Locate every blood parasite and identify its species.
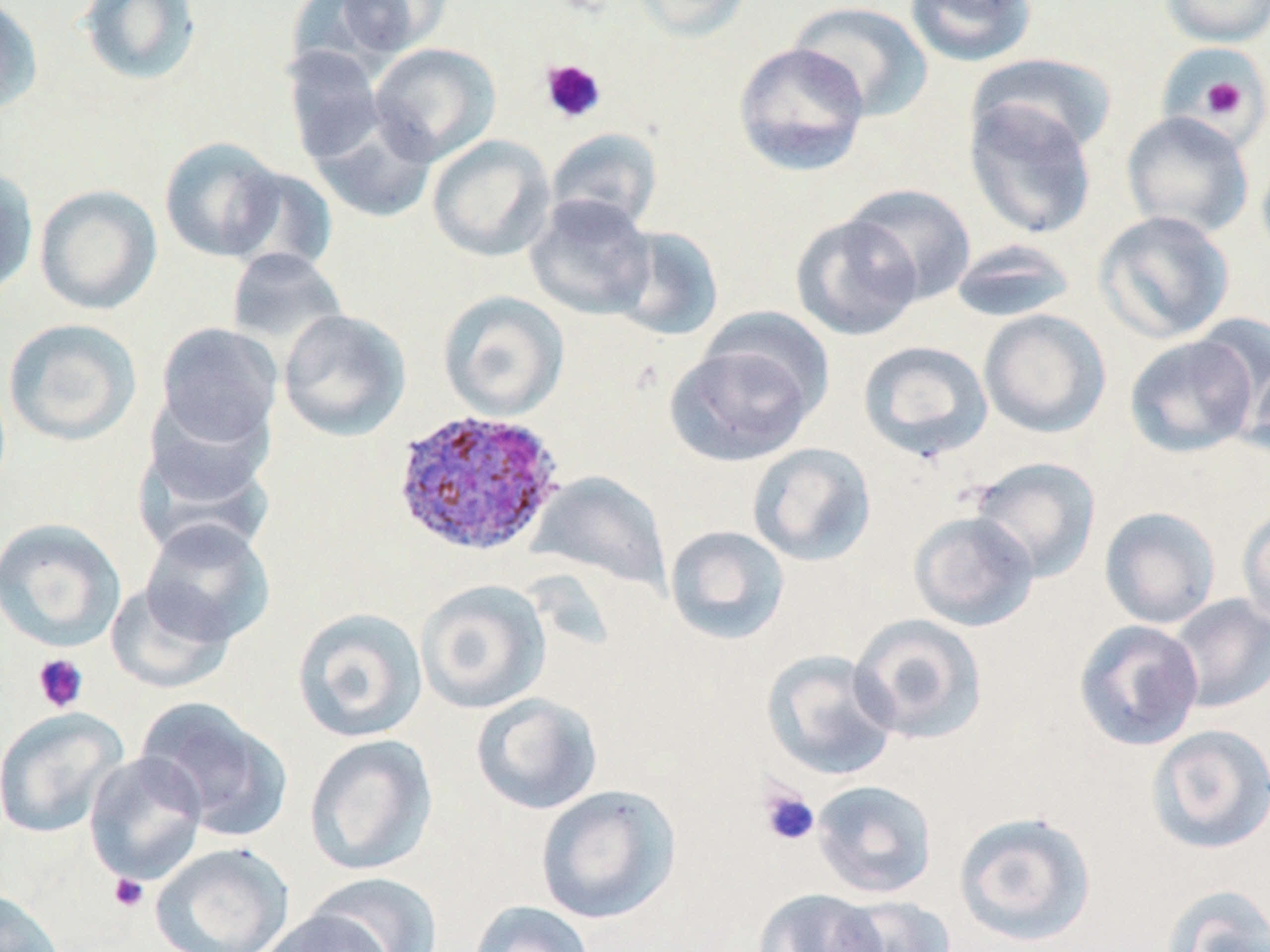

Approximate bounding boxes as (x1, y1, x2, y2) in pixels.
Plasmodium ovale-infected red blood cells: (391, 407, 566, 557).
No Plasmodium falciparum, Plasmodium malariae, Plasmodium vivax, Babesia divergens, or Trypanosoma brucei observed.

slide-level diagnosis = Plasmodium ovale
image size = 1270×952 pixels
magnification = 1000x
platelet locations = approximate bounding boxes as (x1, y1, x2, y2) in pixels: (539, 58, 606, 125), (1197, 75, 1250, 120), (31, 653, 89, 713), (758, 786, 820, 847), (109, 873, 149, 912)
uninfected red blood cell locations = approximate bounding boxes as (x1, y1, x2, y2) in pixels: (76, 0, 202, 87), (333, 0, 450, 58), (630, 0, 754, 42), (904, 0, 1037, 67), (1159, 0, 1270, 47), (0, 1, 43, 117), (787, 1, 933, 122), (369, 42, 501, 165), (733, 42, 870, 177), (282, 46, 387, 164), (1158, 48, 1270, 139), (969, 52, 1118, 158), (963, 97, 1099, 241), (307, 108, 437, 223), (1121, 111, 1255, 239), (545, 127, 663, 233), (427, 135, 556, 262), (159, 136, 285, 262), (1256, 147, 1270, 264), (226, 166, 339, 276), (0, 167, 38, 299), (34, 184, 162, 315), (843, 184, 976, 305), (524, 194, 657, 320), (1094, 210, 1236, 344), (790, 214, 924, 341), (607, 225, 725, 342), (949, 239, 1078, 324), (224, 247, 350, 356), (437, 290, 569, 420), (697, 306, 835, 430), (278, 308, 411, 441), (978, 309, 1111, 438), (1192, 314, 1270, 430), (2, 317, 142, 446), (154, 322, 283, 450), (1124, 332, 1261, 458), (666, 337, 820, 466), (857, 339, 993, 462), (1242, 358, 1270, 459), (136, 401, 278, 534), (747, 442, 876, 567), (967, 456, 1101, 583), (527, 471, 672, 592), (1098, 506, 1222, 629), (1236, 506, 1270, 629), (909, 510, 1039, 632), (0, 517, 126, 652), (139, 518, 274, 647), (664, 525, 790, 645), (415, 579, 551, 714), (105, 580, 236, 695), (1165, 594, 1270, 713), (291, 607, 427, 743), (849, 614, 988, 745), (1073, 619, 1204, 752), (761, 649, 900, 781), (471, 692, 603, 815), (135, 696, 292, 841), (0, 706, 129, 839), (1145, 723, 1270, 855), (304, 734, 438, 876), (83, 751, 209, 887), (810, 779, 938, 899), (535, 784, 681, 924), (952, 809, 1097, 947), (150, 842, 294, 952), (306, 871, 444, 952), (1159, 883, 1270, 952), (0, 888, 67, 952), (752, 888, 888, 952), (833, 895, 956, 952), (467, 900, 596, 952), (256, 907, 395, 952)
preparation = thin blood film
stain = May-Grünwald-Giemsa
modality = optical microscopy
field of view = single